Comment on the morphology of the erythrocytes.
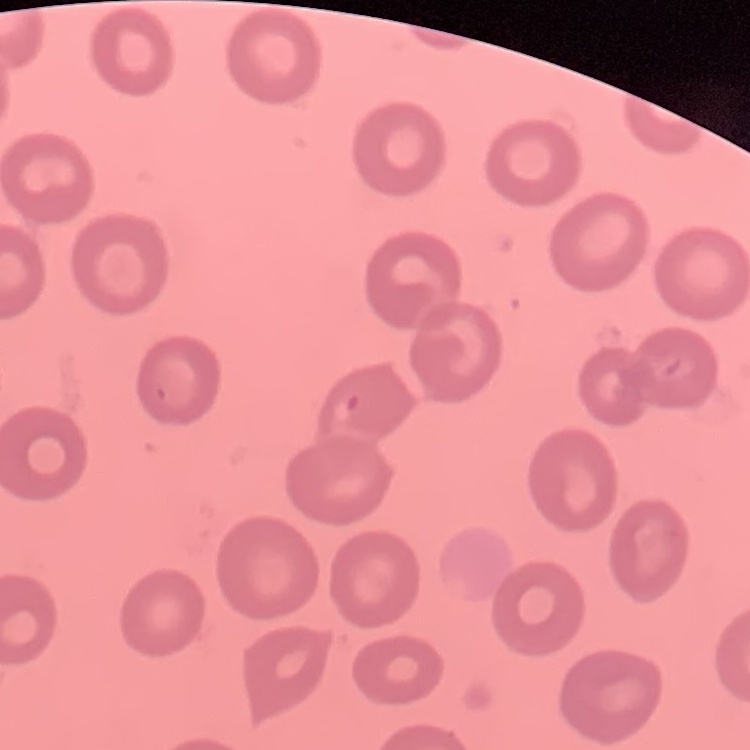

No rouleaux formation.

{
  "stain": "Field's or Giemsa",
  "image_type": "square crop of a larger photomicrograph",
  "preparation": "thin blood smear"
}